Identify the cell.
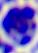
A leukocyte.

Summary:
  - Modality: micrograph
  - Magnification: 400x